Name the blood parasite species.
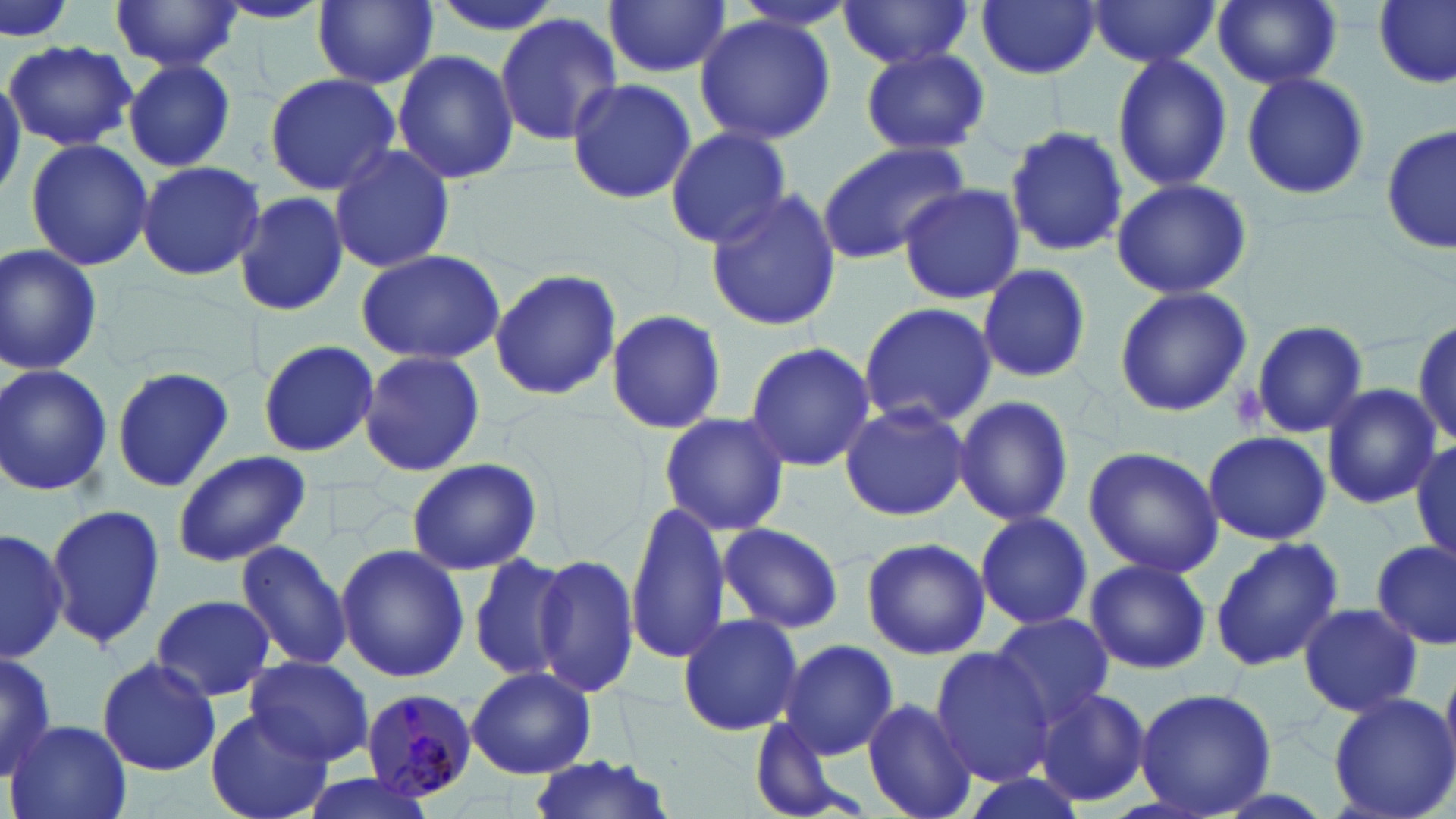
Plasmodium malariae.

Approximate bounding boxes as [x1, y1, x2, y2] in pixels. Uninfected red blood cell locations: [0, 0, 75, 44], [109, 0, 246, 74], [735, 0, 854, 31], [835, 0, 976, 73], [976, 0, 1102, 81], [1086, 0, 1222, 69], [1211, 0, 1346, 90], [1374, 0, 1455, 89], [311, 1, 439, 89], [605, 1, 732, 78], [210, 2, 328, 26], [495, 13, 623, 145], [693, 14, 838, 144], [5, 41, 138, 150], [860, 48, 990, 156], [392, 49, 518, 185], [1110, 51, 1232, 191], [123, 60, 237, 171], [1240, 68, 1370, 202], [263, 72, 403, 195], [565, 78, 696, 207], [1383, 124, 1455, 254], [1004, 126, 1129, 258], [664, 127, 794, 250], [24, 137, 153, 272], [815, 140, 970, 264], [328, 142, 456, 276], [135, 160, 264, 281], [1110, 177, 1253, 301], [897, 185, 1025, 305], [703, 189, 844, 331], [234, 191, 349, 320], [0, 245, 103, 375], [354, 247, 508, 366], [976, 263, 1094, 384], [487, 269, 622, 400], [1115, 285, 1251, 417], [857, 302, 996, 431], [605, 310, 727, 433], [1411, 318, 1456, 448], [1250, 319, 1369, 438], [258, 340, 378, 459], [742, 341, 877, 470], [359, 351, 484, 475], [0, 363, 114, 498], [112, 364, 236, 492], [1320, 382, 1444, 509], [952, 396, 1076, 528], [840, 399, 971, 522], [659, 412, 791, 536], [1201, 431, 1333, 545], [1410, 435, 1456, 564], [1083, 445, 1225, 578], [172, 450, 310, 567], [402, 459, 543, 575], [44, 501, 167, 654], [625, 501, 731, 664], [974, 509, 1093, 631], [717, 522, 843, 634], [0, 529, 68, 665], [1208, 534, 1344, 672], [859, 537, 990, 659], [232, 539, 356, 673], [1371, 539, 1455, 651], [335, 543, 470, 684], [466, 552, 578, 685], [536, 554, 642, 698], [1083, 558, 1210, 676], [152, 592, 276, 703], [1298, 603, 1423, 715], [676, 611, 805, 737], [986, 612, 1117, 729], [778, 640, 900, 759], [0, 646, 58, 786], [929, 647, 1059, 785], [243, 655, 375, 766], [95, 656, 222, 776], [467, 668, 596, 779], [1033, 687, 1154, 811], [1133, 688, 1278, 817], [1326, 693, 1456, 819], [862, 697, 976, 818], [206, 710, 333, 819], [749, 715, 854, 818], [8, 719, 133, 819], [523, 755, 678, 819], [293, 775, 439, 819]. Platelet locations: [1232, 379, 1268, 430]. Plasmodium malariae-infected red blood cell locations: [361, 687, 479, 803]. Optical microscopy. Thin blood film. Captured at 1000x magnification. Single field of view. Image is 1456×819 pixels. May-Grünwald-Giemsa-stained preparation.